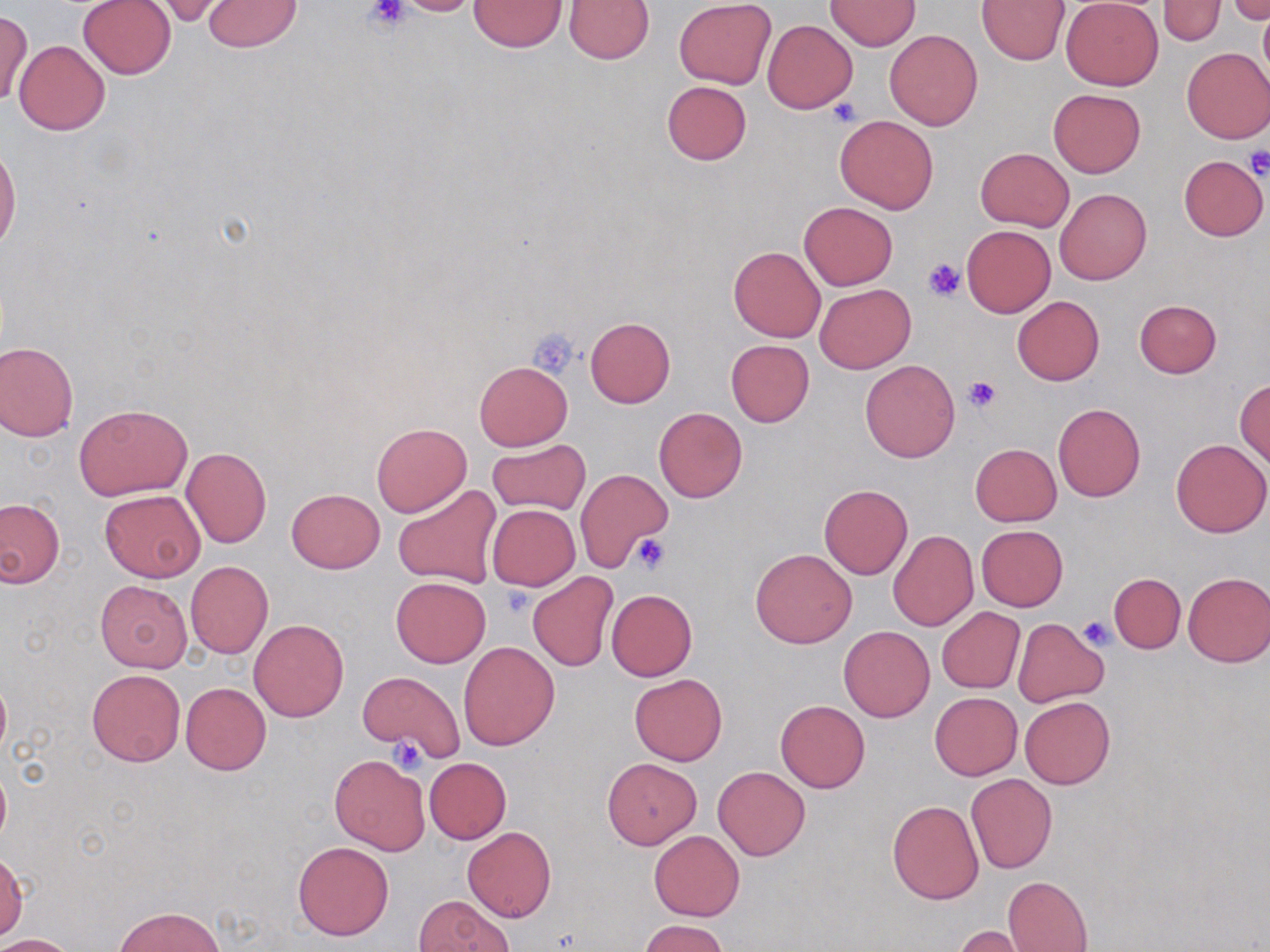

Summary:
  - Coordinate format: approximate bounding boxes as named x1/y1/x2/y2 corners in pixels
  - Uninfected red blood cell locations: (x1=388, y1=0, x2=486, y2=17), (x1=977, y1=0, x2=1070, y2=65), (x1=1061, y1=0, x2=1163, y2=89), (x1=1159, y1=0, x2=1225, y2=45), (x1=1227, y1=0, x2=1269, y2=24), (x1=77, y1=1, x2=176, y2=78), (x1=202, y1=1, x2=302, y2=51), (x1=469, y1=1, x2=568, y2=52), (x1=563, y1=1, x2=655, y2=63), (x1=674, y1=1, x2=776, y2=88), (x1=824, y1=1, x2=922, y2=51), (x1=148, y1=2, x2=230, y2=26), (x1=1258, y1=8, x2=1270, y2=89), (x1=1, y1=9, x2=32, y2=107), (x1=763, y1=20, x2=858, y2=113), (x1=885, y1=29, x2=983, y2=130), (x1=14, y1=40, x2=110, y2=136), (x1=1181, y1=47, x2=1270, y2=143), (x1=661, y1=81, x2=751, y2=165), (x1=1048, y1=88, x2=1145, y2=177), (x1=834, y1=114, x2=940, y2=214), (x1=0, y1=144, x2=20, y2=257), (x1=975, y1=147, x2=1074, y2=230), (x1=1177, y1=154, x2=1268, y2=241), (x1=1055, y1=189, x2=1153, y2=285), (x1=799, y1=202, x2=897, y2=290), (x1=962, y1=226, x2=1054, y2=317), (x1=728, y1=245, x2=825, y2=341), (x1=815, y1=284, x2=915, y2=373), (x1=1012, y1=295, x2=1104, y2=385), (x1=1134, y1=299, x2=1222, y2=378), (x1=585, y1=316, x2=676, y2=407), (x1=725, y1=339, x2=814, y2=427), (x1=0, y1=341, x2=79, y2=442), (x1=860, y1=360, x2=960, y2=462), (x1=473, y1=361, x2=572, y2=451), (x1=1235, y1=380, x2=1269, y2=468), (x1=74, y1=403, x2=192, y2=500), (x1=1052, y1=403, x2=1146, y2=502), (x1=655, y1=408, x2=748, y2=502), (x1=370, y1=422, x2=471, y2=517), (x1=1170, y1=438, x2=1269, y2=538), (x1=487, y1=439, x2=591, y2=515), (x1=971, y1=443, x2=1061, y2=526), (x1=181, y1=447, x2=272, y2=548), (x1=575, y1=469, x2=671, y2=572), (x1=393, y1=484, x2=501, y2=590), (x1=820, y1=484, x2=913, y2=579), (x1=286, y1=489, x2=385, y2=574), (x1=100, y1=491, x2=205, y2=581), (x1=0, y1=497, x2=66, y2=588), (x1=487, y1=504, x2=581, y2=590), (x1=853, y1=514, x2=948, y2=633), (x1=977, y1=525, x2=1067, y2=610), (x1=887, y1=530, x2=978, y2=631), (x1=750, y1=548, x2=857, y2=648), (x1=185, y1=560, x2=273, y2=658), (x1=1182, y1=571, x2=1269, y2=667), (x1=528, y1=572, x2=618, y2=671), (x1=1108, y1=573, x2=1186, y2=654), (x1=390, y1=576, x2=491, y2=668), (x1=95, y1=579, x2=193, y2=672), (x1=606, y1=589, x2=697, y2=681), (x1=937, y1=607, x2=1024, y2=693), (x1=250, y1=619, x2=348, y2=722), (x1=1012, y1=619, x2=1108, y2=707), (x1=838, y1=625, x2=935, y2=722), (x1=458, y1=642, x2=559, y2=750), (x1=87, y1=669, x2=185, y2=766), (x1=357, y1=671, x2=465, y2=761), (x1=0, y1=673, x2=11, y2=763), (x1=630, y1=673, x2=727, y2=767), (x1=181, y1=683, x2=270, y2=775), (x1=930, y1=692, x2=1022, y2=780), (x1=1020, y1=695, x2=1115, y2=789), (x1=775, y1=700, x2=869, y2=793), (x1=329, y1=754, x2=429, y2=854), (x1=602, y1=757, x2=701, y2=848), (x1=424, y1=758, x2=512, y2=843), (x1=0, y1=762, x2=10, y2=850), (x1=713, y1=766, x2=809, y2=860), (x1=966, y1=773, x2=1057, y2=873), (x1=887, y1=800, x2=983, y2=905), (x1=463, y1=827, x2=556, y2=922), (x1=649, y1=831, x2=744, y2=921), (x1=294, y1=841, x2=394, y2=941), (x1=0, y1=853, x2=26, y2=940), (x1=1003, y1=876, x2=1093, y2=951), (x1=415, y1=895, x2=513, y2=952), (x1=115, y1=906, x2=223, y2=950), (x1=640, y1=919, x2=727, y2=952), (x1=952, y1=925, x2=1035, y2=952), (x1=0, y1=933, x2=80, y2=952)
  - Platelet locations: (x1=363, y1=1, x2=409, y2=35), (x1=827, y1=96, x2=863, y2=128), (x1=1243, y1=147, x2=1270, y2=180), (x1=923, y1=257, x2=967, y2=300), (x1=528, y1=327, x2=582, y2=379), (x1=962, y1=375, x2=1002, y2=412), (x1=629, y1=532, x2=671, y2=575), (x1=498, y1=584, x2=532, y2=617), (x1=1077, y1=615, x2=1116, y2=651), (x1=387, y1=738, x2=428, y2=774)
  - Slide-level diagnosis: negative for blood parasites
  - Preparation: thin blood smear
  - Field of view: single
  - Image size: 1270×952 pixels
  - Magnification: 1000x
  - Modality: light microscopy
  - Stain: May-Grünwald-Giemsa